Identify the blood parasite species.
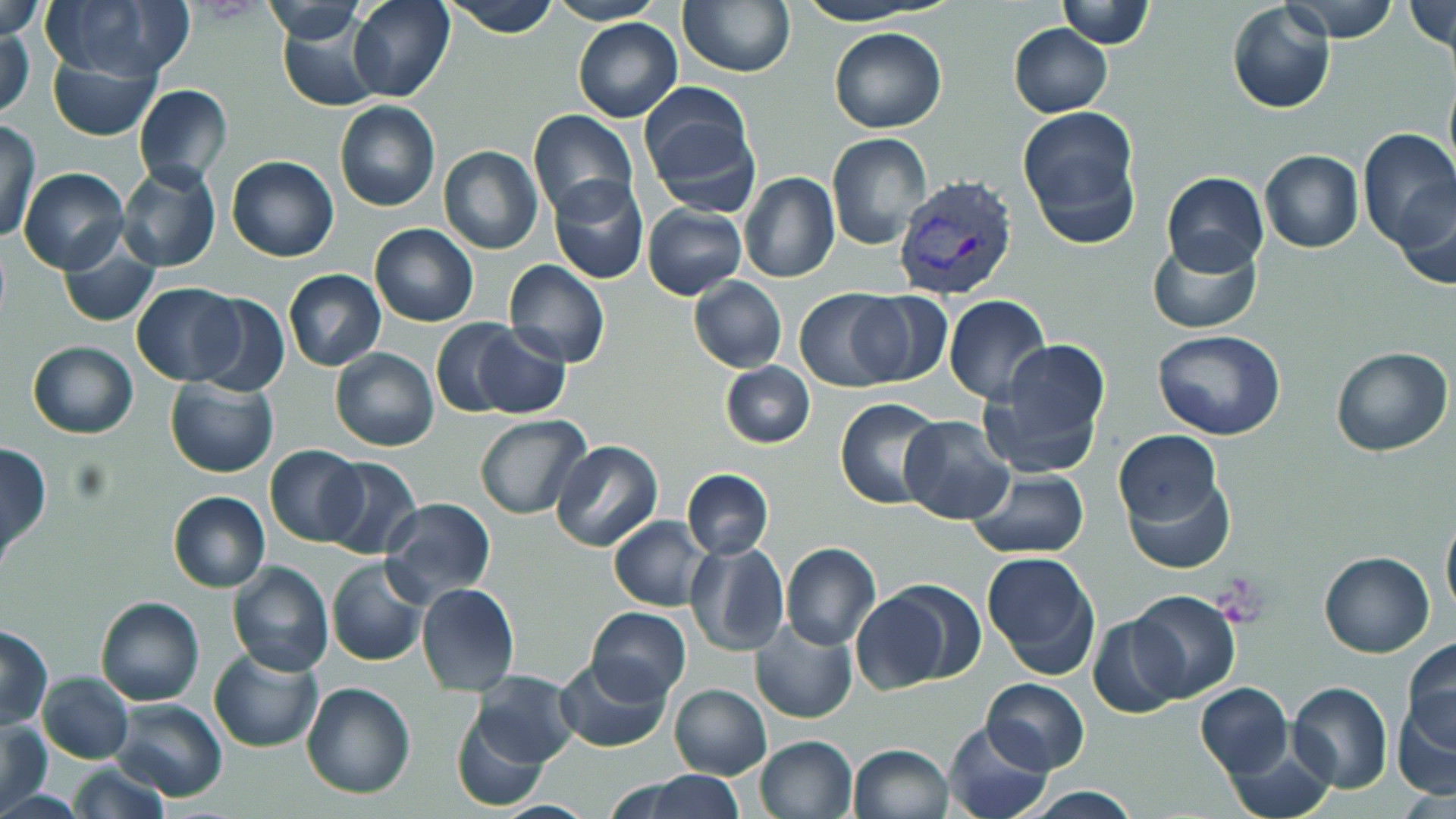
Plasmodium vivax.

Approximate bounding boxes as [x1, y1, x2, y2] in pixels. Plasmodium vivax-infected red blood cell locations: [894, 173, 1020, 303]. Platelet locations: [1216, 580, 1268, 622]. Uninfected red blood cell locations: [349, 0, 455, 103], [443, 0, 562, 38], [678, 0, 796, 78], [791, 0, 940, 25], [1056, 0, 1154, 47], [1282, 0, 1400, 42], [39, 1, 190, 81], [256, 1, 371, 42], [547, 1, 666, 24], [0, 2, 45, 43], [1226, 2, 1335, 115], [1404, 3, 1455, 54], [277, 16, 384, 112], [573, 18, 682, 121], [0, 23, 34, 120], [1009, 24, 1112, 116], [828, 26, 947, 133], [47, 50, 161, 142], [1443, 73, 1456, 179], [133, 84, 233, 189], [638, 84, 763, 217], [333, 101, 440, 213], [1018, 107, 1143, 246], [529, 110, 637, 222], [0, 119, 42, 245], [1356, 129, 1456, 253], [826, 132, 934, 252], [437, 146, 543, 255], [1260, 150, 1362, 253], [227, 155, 339, 263], [116, 163, 221, 273], [18, 167, 129, 275], [738, 172, 840, 286], [1160, 172, 1268, 276], [548, 173, 649, 284], [1394, 175, 1456, 290], [642, 203, 747, 299], [369, 223, 479, 327], [1148, 236, 1261, 334], [58, 238, 160, 328], [503, 258, 610, 369], [283, 270, 385, 371], [687, 277, 787, 373], [132, 282, 245, 384], [794, 287, 905, 393], [849, 291, 951, 387], [189, 292, 289, 398], [942, 295, 1050, 405], [430, 319, 521, 418], [469, 323, 571, 419], [1153, 329, 1285, 440], [980, 338, 1113, 480], [27, 341, 138, 438], [1330, 346, 1452, 457], [330, 347, 441, 451], [721, 361, 815, 448], [165, 378, 279, 478], [835, 397, 945, 509], [475, 414, 592, 521], [899, 415, 1015, 524], [1114, 432, 1223, 531], [551, 440, 663, 554], [0, 443, 51, 560], [264, 446, 365, 546], [321, 456, 422, 557], [1121, 466, 1235, 574], [682, 468, 774, 560], [966, 468, 1092, 558], [168, 490, 270, 593], [381, 497, 496, 604], [1440, 508, 1456, 622], [608, 515, 713, 611], [685, 542, 788, 657], [781, 542, 881, 651], [981, 551, 1102, 681], [1319, 551, 1435, 658], [327, 558, 429, 667], [227, 560, 333, 676], [416, 582, 520, 698], [851, 585, 974, 694], [1129, 589, 1241, 703], [96, 597, 203, 705], [587, 606, 691, 701], [1086, 615, 1189, 719], [751, 618, 857, 724], [0, 626, 51, 727], [1402, 637, 1456, 753], [208, 648, 322, 752], [553, 657, 672, 752], [472, 670, 581, 768], [37, 671, 134, 765], [981, 678, 1090, 773], [300, 682, 416, 800], [1193, 682, 1292, 778], [1287, 682, 1393, 793], [670, 684, 771, 780], [1393, 692, 1456, 801], [111, 698, 227, 801], [450, 710, 551, 810], [0, 718, 52, 815], [942, 719, 1055, 819], [754, 735, 858, 819], [1223, 737, 1338, 819], [848, 742, 954, 818], [64, 762, 171, 818], [640, 772, 745, 818], [1015, 787, 1147, 819]. Thin blood smear. Single field of view. May-Grünwald-Giemsa stain. Captured at 1000x magnification. Image is 1456×819 pixels. Optical microscopy.